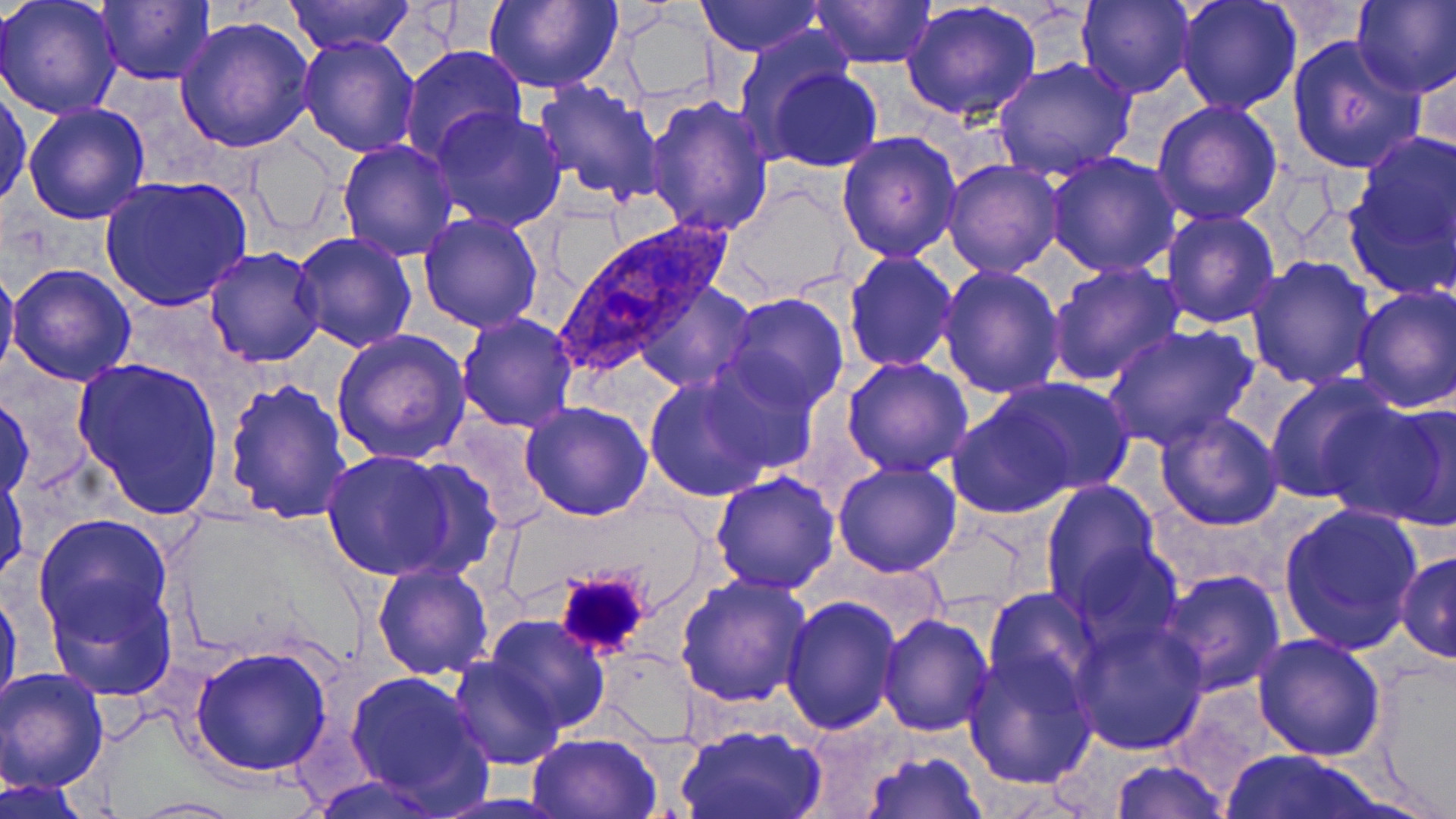

{
  "plasmodium_ovale_infected_red_blood_cell_locations": "approximate bounding boxes as named x1/y1/x2/y2 corners in pixels: (x1=556, y1=221, x2=737, y2=381)",
  "slide_level_diagnosis": "Plasmodium ovale",
  "image_size": "1456×819 pixels",
  "uninfected_red_blood_cell_locations": "approximate bounding boxes as named x1/y1/x2/y2 corners in pixels: (x1=1, y1=0, x2=123, y2=121), (x1=97, y1=0, x2=216, y2=85), (x1=285, y1=0, x2=415, y2=53), (x1=483, y1=0, x2=622, y2=92), (x1=694, y1=0, x2=822, y2=55), (x1=809, y1=0, x2=934, y2=68), (x1=1077, y1=0, x2=1195, y2=100), (x1=1175, y1=0, x2=1303, y2=115), (x1=1353, y1=1, x2=1455, y2=97), (x1=901, y1=2, x2=1041, y2=122), (x1=612, y1=9, x2=719, y2=103), (x1=174, y1=17, x2=316, y2=156), (x1=734, y1=26, x2=855, y2=145), (x1=298, y1=32, x2=421, y2=157), (x1=1286, y1=35, x2=1426, y2=175), (x1=400, y1=44, x2=529, y2=166), (x1=1414, y1=50, x2=1455, y2=165), (x1=991, y1=57, x2=1139, y2=182), (x1=762, y1=64, x2=884, y2=172), (x1=531, y1=79, x2=667, y2=205), (x1=0, y1=85, x2=32, y2=210), (x1=644, y1=92, x2=775, y2=235), (x1=1151, y1=99, x2=1283, y2=226), (x1=21, y1=101, x2=152, y2=224), (x1=431, y1=103, x2=567, y2=232), (x1=1346, y1=128, x2=1454, y2=286), (x1=837, y1=131, x2=962, y2=263), (x1=241, y1=133, x2=340, y2=240), (x1=336, y1=140, x2=458, y2=261), (x1=1044, y1=152, x2=1184, y2=278), (x1=942, y1=159, x2=1066, y2=278), (x1=99, y1=174, x2=252, y2=311), (x1=727, y1=184, x2=853, y2=297), (x1=1159, y1=209, x2=1283, y2=328), (x1=418, y1=211, x2=546, y2=333), (x1=291, y1=232, x2=419, y2=354), (x1=204, y1=246, x2=325, y2=368), (x1=844, y1=251, x2=957, y2=373), (x1=1245, y1=255, x2=1378, y2=391), (x1=0, y1=258, x2=20, y2=386), (x1=1047, y1=261, x2=1186, y2=388), (x1=6, y1=262, x2=137, y2=386), (x1=937, y1=263, x2=1067, y2=399), (x1=636, y1=280, x2=754, y2=393), (x1=1350, y1=284, x2=1455, y2=413), (x1=725, y1=292, x2=848, y2=413), (x1=457, y1=312, x2=580, y2=432), (x1=1102, y1=322, x2=1260, y2=451), (x1=331, y1=330, x2=471, y2=466), (x1=69, y1=354, x2=226, y2=522), (x1=841, y1=356, x2=974, y2=476), (x1=698, y1=357, x2=819, y2=475), (x1=1261, y1=372, x2=1401, y2=503), (x1=643, y1=375, x2=775, y2=501), (x1=221, y1=378, x2=352, y2=525), (x1=995, y1=378, x2=1138, y2=495), (x1=0, y1=393, x2=35, y2=504), (x1=1341, y1=395, x2=1456, y2=531), (x1=520, y1=401, x2=654, y2=520), (x1=946, y1=402, x2=1074, y2=518), (x1=1154, y1=410, x2=1284, y2=531), (x1=444, y1=419, x2=554, y2=527), (x1=320, y1=450, x2=459, y2=580), (x1=391, y1=457, x2=502, y2=583), (x1=833, y1=461, x2=962, y2=578), (x1=710, y1=469, x2=840, y2=594), (x1=1, y1=473, x2=28, y2=584), (x1=1038, y1=479, x2=1166, y2=618), (x1=1277, y1=502, x2=1425, y2=654), (x1=33, y1=514, x2=172, y2=643), (x1=1066, y1=545, x2=1182, y2=655), (x1=1395, y1=546, x2=1455, y2=668), (x1=371, y1=563, x2=493, y2=680), (x1=1156, y1=568, x2=1289, y2=697), (x1=675, y1=573, x2=814, y2=708), (x1=1, y1=580, x2=21, y2=720), (x1=45, y1=580, x2=178, y2=703), (x1=984, y1=588, x2=1102, y2=704), (x1=781, y1=596, x2=901, y2=736), (x1=878, y1=613, x2=996, y2=737), (x1=484, y1=614, x2=614, y2=733), (x1=1068, y1=616, x2=1210, y2=757), (x1=1252, y1=631, x2=1386, y2=761), (x1=188, y1=643, x2=335, y2=777), (x1=961, y1=649, x2=1098, y2=789), (x1=1365, y1=655, x2=1456, y2=815), (x1=447, y1=656, x2=565, y2=770), (x1=1, y1=667, x2=111, y2=795), (x1=345, y1=668, x2=492, y2=811), (x1=675, y1=724, x2=827, y2=819), (x1=526, y1=733, x2=662, y2=818), (x1=859, y1=748, x2=986, y2=819), (x1=1221, y1=748, x2=1388, y2=818), (x1=1109, y1=759, x2=1232, y2=818), (x1=308, y1=773, x2=450, y2=817), (x1=2, y1=776, x2=91, y2=816), (x1=124, y1=796, x2=244, y2=817)",
  "magnification": "1000x",
  "field_of_view": "one of a larger specimen",
  "platelet_locations": "approximate bounding boxes as named x1/y1/x2/y2 corners in pixels: (x1=552, y1=567, x2=654, y2=661)",
  "modality": "light microscopy",
  "stain": "May-Grünwald-Giemsa",
  "preparation": "thin blood film"
}